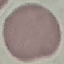

Summary:
  - Malaria status: uninfected
  - Stain: Giemsa
  - Preparation: thin blood smear
  - Capture: smartphone camera at the microscope eyepiece
  - Image type: cell patch, automatically extracted from a larger field of view and resized to 64 × 64 pixels